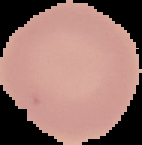

From a thin blood film. Result: negative for malaria parasites. Image is 142×145 pixels. Cell region segmented out of the field of view; the surrounding area is masked to black.